Locate and identify every blood parasite.
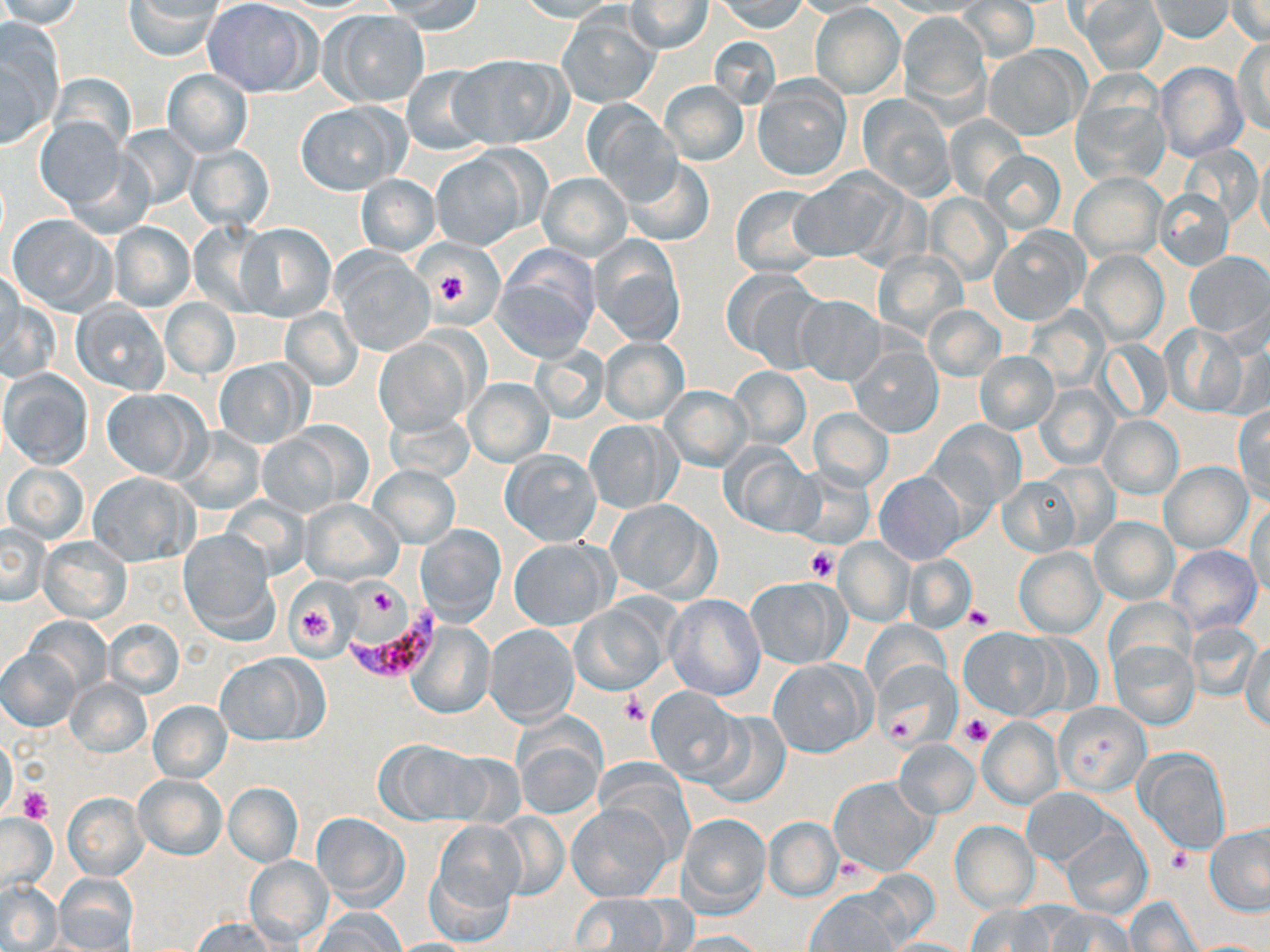
Approximate bounding boxes as [x1, y1, x2, y2] in pixels.
Plasmodium falciparum-infected red blood cells: [350, 605, 446, 681].
No Plasmodium ovale, Plasmodium malariae, Plasmodium vivax, Babesia divergens, or Trypanosoma brucei observed.

Platelet locations: [436, 270, 468, 303], [807, 548, 838, 583], [363, 586, 401, 619], [290, 601, 338, 651], [965, 605, 992, 629], [621, 693, 646, 725], [884, 713, 917, 742], [959, 713, 994, 746], [18, 787, 50, 823], [1167, 848, 1193, 873]. Uninfected red blood cell locations: [0, 0, 86, 28], [125, 0, 222, 62], [202, 0, 316, 97], [383, 0, 486, 35], [514, 0, 621, 22], [717, 0, 807, 33], [878, 0, 990, 17], [1077, 0, 1167, 74], [1149, 0, 1233, 41], [624, 1, 715, 53], [791, 1, 883, 18], [956, 1, 1038, 63], [1228, 1, 1269, 44], [811, 3, 905, 98], [321, 9, 429, 107], [899, 12, 990, 113], [559, 13, 658, 108], [0, 22, 65, 144], [1235, 36, 1269, 136], [985, 46, 1086, 141], [451, 52, 572, 149], [1155, 60, 1248, 162], [401, 65, 491, 156], [163, 68, 253, 156], [46, 73, 137, 156], [751, 78, 852, 182], [659, 80, 749, 166], [1071, 86, 1169, 188], [857, 94, 956, 202], [581, 100, 680, 201], [298, 102, 407, 194], [944, 114, 1026, 199], [35, 117, 129, 212], [115, 123, 201, 211], [185, 145, 274, 231], [1256, 150, 1270, 245], [430, 151, 529, 251], [979, 151, 1066, 234], [621, 157, 715, 247], [1071, 172, 1164, 262], [538, 173, 631, 260], [790, 173, 900, 264], [356, 175, 439, 257], [730, 185, 828, 279], [1154, 188, 1234, 270], [927, 194, 1007, 284], [7, 214, 117, 316], [186, 220, 274, 318], [110, 222, 195, 312], [235, 223, 336, 323], [989, 225, 1090, 325], [590, 236, 686, 346], [493, 246, 601, 359], [873, 250, 968, 341], [1081, 250, 1167, 346], [331, 251, 434, 355], [1185, 251, 1269, 340], [1, 266, 23, 361], [723, 270, 820, 369], [3, 288, 56, 384], [795, 295, 887, 385], [161, 297, 239, 380], [71, 301, 170, 395], [280, 306, 364, 391], [924, 306, 1004, 382], [1159, 323, 1249, 417], [375, 336, 476, 437], [598, 337, 688, 424], [1098, 340, 1171, 421], [848, 343, 943, 438], [530, 346, 610, 423], [975, 353, 1058, 433], [214, 358, 312, 448], [727, 368, 810, 450], [0, 370, 93, 471], [463, 377, 555, 469], [1034, 384, 1117, 470], [661, 386, 752, 471], [100, 388, 208, 482], [1234, 405, 1270, 503], [808, 408, 893, 491], [384, 409, 475, 483], [1099, 415, 1183, 499], [582, 419, 678, 515], [928, 419, 1025, 512], [257, 425, 359, 517], [174, 428, 266, 515], [721, 444, 818, 537], [500, 449, 601, 546], [1159, 461, 1253, 552], [3, 463, 88, 544], [369, 465, 461, 547], [788, 467, 874, 549], [90, 471, 199, 566], [873, 472, 965, 565], [996, 476, 1081, 556], [1246, 496, 1270, 600], [218, 497, 311, 579], [301, 497, 404, 585], [604, 499, 719, 602], [1089, 517, 1177, 605], [0, 524, 51, 606], [415, 524, 504, 626], [177, 530, 278, 639], [38, 535, 131, 624], [834, 536, 915, 626], [507, 537, 615, 630], [1167, 545, 1261, 635], [1015, 547, 1104, 637], [902, 555, 974, 632], [746, 577, 847, 669], [664, 593, 765, 700], [1104, 597, 1195, 679], [571, 603, 669, 694], [24, 616, 112, 694], [105, 618, 184, 698], [407, 620, 494, 719], [864, 620, 949, 702], [1185, 622, 1263, 702], [485, 624, 578, 725], [959, 628, 1054, 718], [1110, 637, 1199, 730], [1241, 642, 1270, 732], [2, 650, 81, 730], [872, 651, 957, 752], [215, 653, 323, 746], [769, 658, 873, 757], [66, 679, 152, 756], [644, 686, 743, 783], [148, 701, 232, 782], [1054, 703, 1149, 795], [701, 709, 791, 805], [978, 718, 1062, 808], [513, 720, 606, 821], [894, 738, 979, 818], [0, 739, 19, 819], [377, 740, 482, 823], [1136, 751, 1230, 857], [593, 763, 696, 850], [134, 773, 226, 859], [829, 776, 936, 874], [224, 783, 302, 866], [1021, 788, 1115, 869], [62, 792, 148, 881], [568, 802, 670, 902], [311, 811, 408, 910], [676, 812, 771, 915], [487, 813, 570, 900], [0, 814, 57, 897], [431, 818, 527, 919], [764, 818, 841, 901], [950, 821, 1037, 911], [1205, 825, 1270, 916], [1060, 827, 1152, 919], [424, 852, 517, 949], [245, 856, 334, 946], [54, 871, 140, 950], [0, 883, 62, 950], [806, 891, 901, 952], [572, 892, 676, 951], [1126, 895, 1202, 952], [966, 902, 1058, 952], [1042, 907, 1136, 952], [311, 909, 404, 952], [192, 917, 284, 951], [675, 930, 767, 952], [881, 937, 976, 952]. Slide-level diagnosis: Plasmodium falciparum. One field of a larger specimen. 1000x magnification. Image is 1270×952 pixels. Thin blood smear. Light microscopy. May-Grünwald-Giemsa-stained preparation.